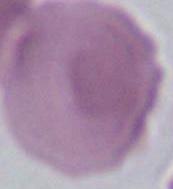

Captured at 1000x magnification. Micrograph. An erythrocyte is seen.